Point out each Plasmodium parasite.
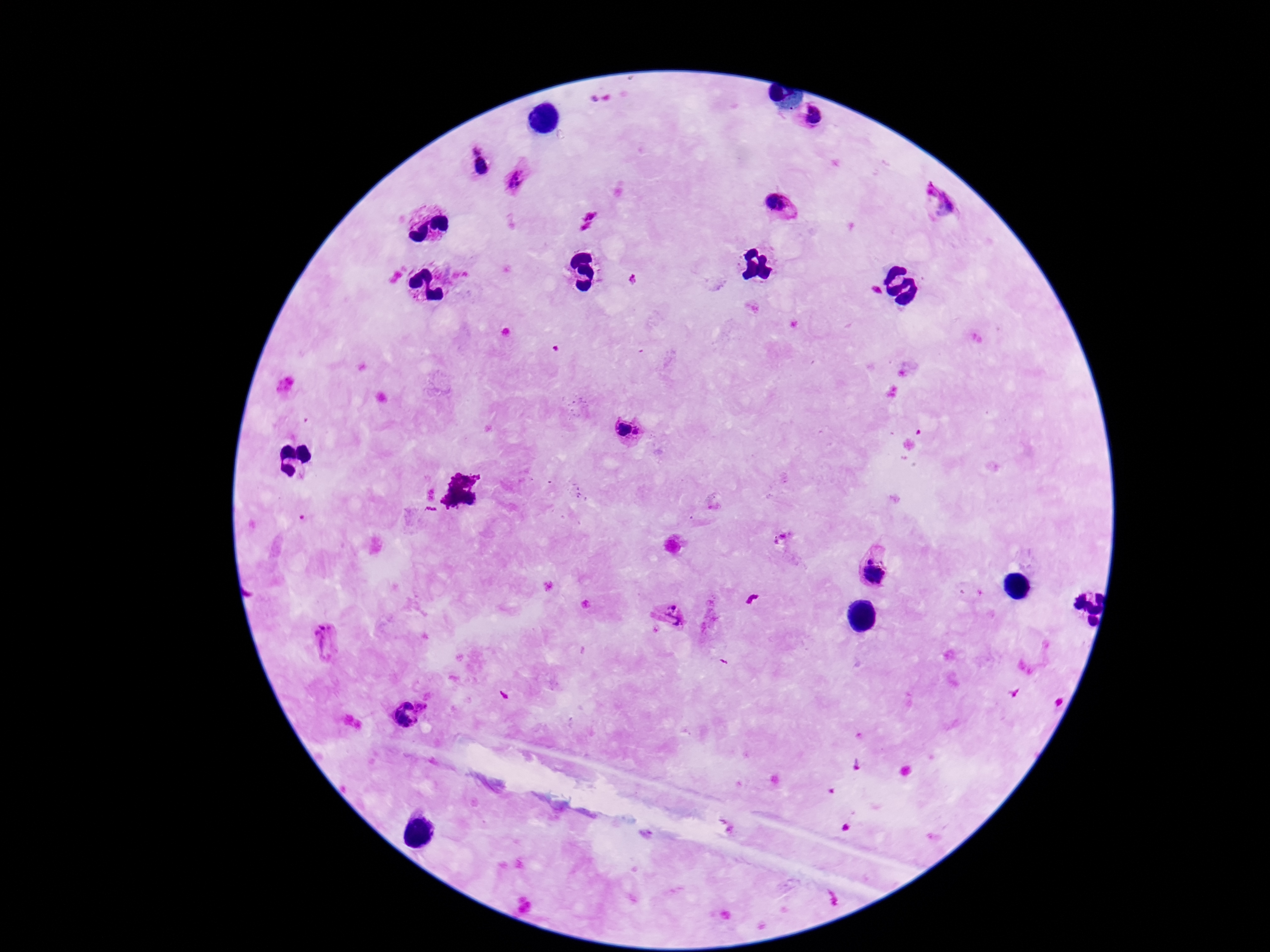
Approximate object centers, in pixels from the top-left corner.
Plasmodium parasites: (x=812, y=115), (x=476, y=149), (x=482, y=166), (x=519, y=178), (x=937, y=201), (x=779, y=204), (x=623, y=428), (x=639, y=431), (x=871, y=558), (x=873, y=576), (x=673, y=607), (x=670, y=621), (x=325, y=641), (x=407, y=706), (x=422, y=706), (x=402, y=721).

Single field of view. Smartphone photograph taken through the microscope eyepiece. Patient malaria status: infected. 100x magnification. Image is 1270×952 pixels. Thick blood smear. Giemsa stain.